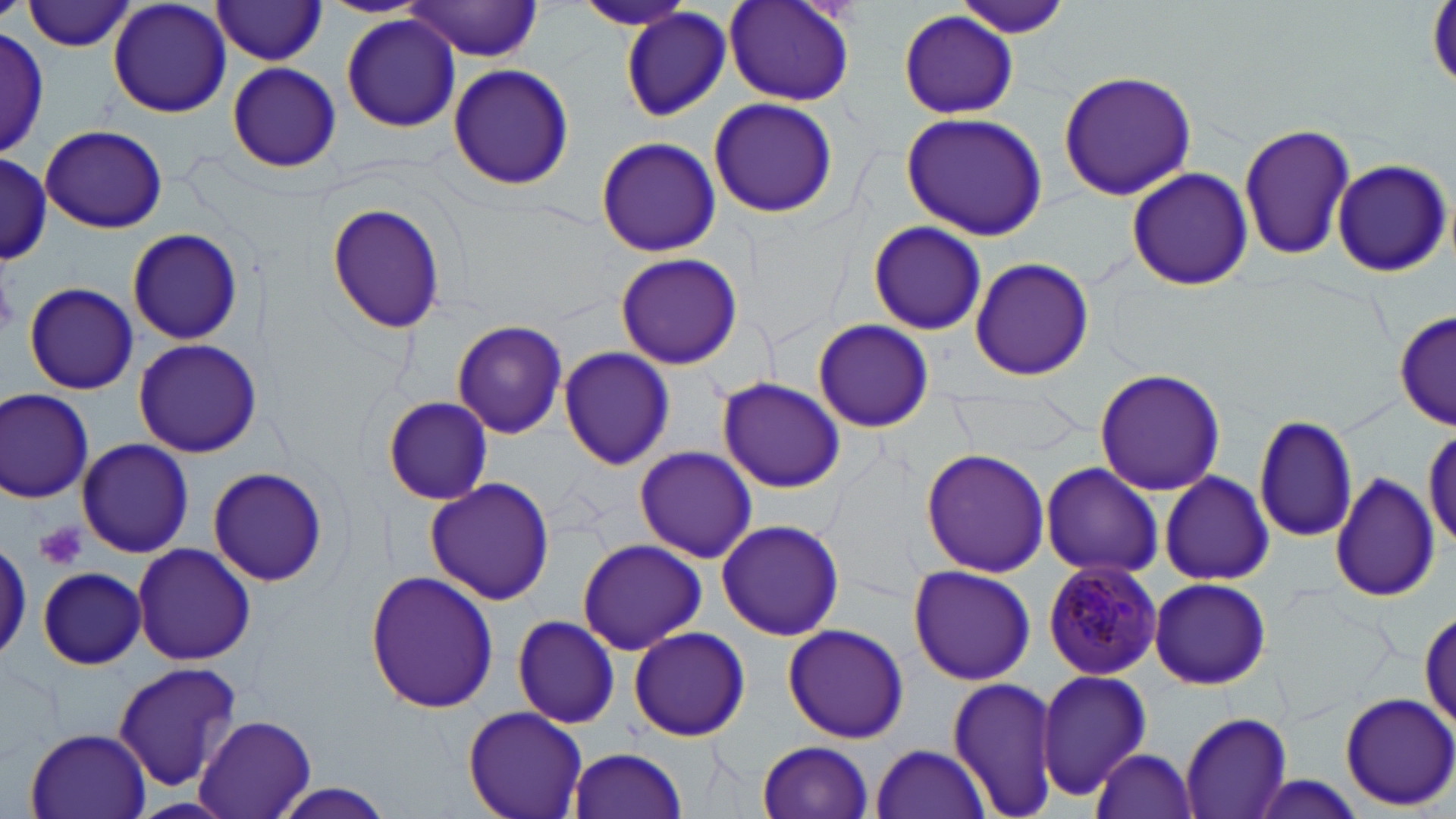
Summary:
  - Coordinate format: approximate bounding boxes as (x1, y1, x2, y2) in pixels
  - Platelet locations: (0, 273, 21, 336), (36, 521, 86, 572)
  - Plasmodium malariae-infected red blood cell locations: (1042, 558, 1164, 680)
  - Uninfected red blood cell locations: (723, 0, 858, 106), (24, 1, 138, 52), (108, 1, 233, 120), (954, 1, 1074, 39), (209, 2, 329, 65), (571, 2, 697, 31), (400, 3, 548, 63), (622, 8, 731, 122), (897, 9, 1022, 120), (341, 15, 462, 131), (0, 29, 50, 158), (227, 62, 340, 173), (446, 63, 575, 192), (1057, 69, 1200, 199), (707, 97, 840, 219), (899, 112, 1047, 241), (1240, 123, 1356, 260), (41, 125, 169, 234), (595, 135, 723, 258), (1, 153, 51, 263), (1330, 159, 1451, 277), (1125, 168, 1251, 291), (326, 201, 449, 334), (867, 220, 989, 334), (127, 227, 244, 346), (614, 252, 742, 369), (968, 256, 1095, 382), (23, 281, 138, 394), (1394, 311, 1456, 430), (810, 319, 935, 430), (450, 320, 568, 439), (133, 339, 262, 458), (556, 347, 676, 469), (1093, 368, 1226, 496), (718, 376, 845, 493), (0, 390, 93, 501), (382, 396, 493, 505), (1249, 413, 1361, 542), (76, 439, 192, 557), (634, 446, 757, 564), (920, 448, 1050, 578), (1038, 462, 1164, 579), (207, 467, 328, 586), (1157, 469, 1275, 586), (1330, 472, 1441, 603), (424, 476, 556, 607), (715, 518, 845, 641), (576, 537, 707, 654), (0, 539, 33, 659), (132, 542, 256, 665), (908, 564, 1036, 685), (36, 567, 148, 669), (365, 568, 500, 713), (1147, 576, 1272, 690), (512, 613, 621, 728), (781, 625, 909, 744), (626, 627, 751, 741), (111, 662, 243, 791), (1035, 670, 1152, 798), (947, 675, 1061, 819), (1339, 690, 1456, 812), (463, 704, 590, 819), (1179, 712, 1293, 819), (194, 714, 316, 818), (23, 728, 154, 819), (755, 741, 876, 819), (869, 744, 991, 819), (568, 748, 689, 818), (1090, 750, 1200, 819), (1243, 777, 1370, 819), (263, 782, 403, 818)
  - Slide-level diagnosis: Plasmodium malariae
  - Preparation: thin blood smear
  - Image size: 1456×819 pixels
  - Field of view: single
  - Magnification: 1000x
  - Stain: May-Grünwald-Giemsa
  - Modality: light microscopy